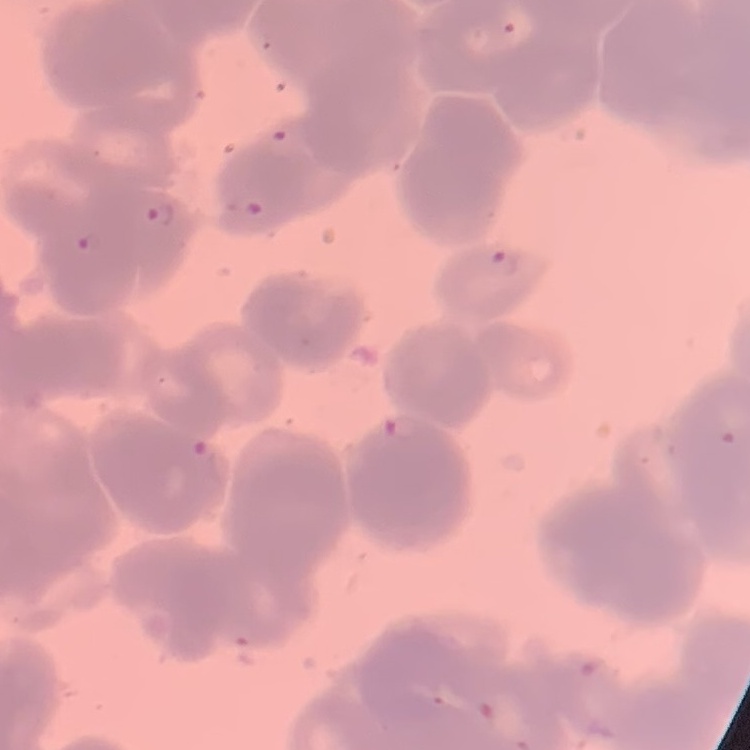

Summary:
  - Red blood cell morphology: rouleaux formation
  - Stain: Field's or Giemsa
  - Image type: one tile cut from a larger photomicrograph
  - Preparation: thin blood smear